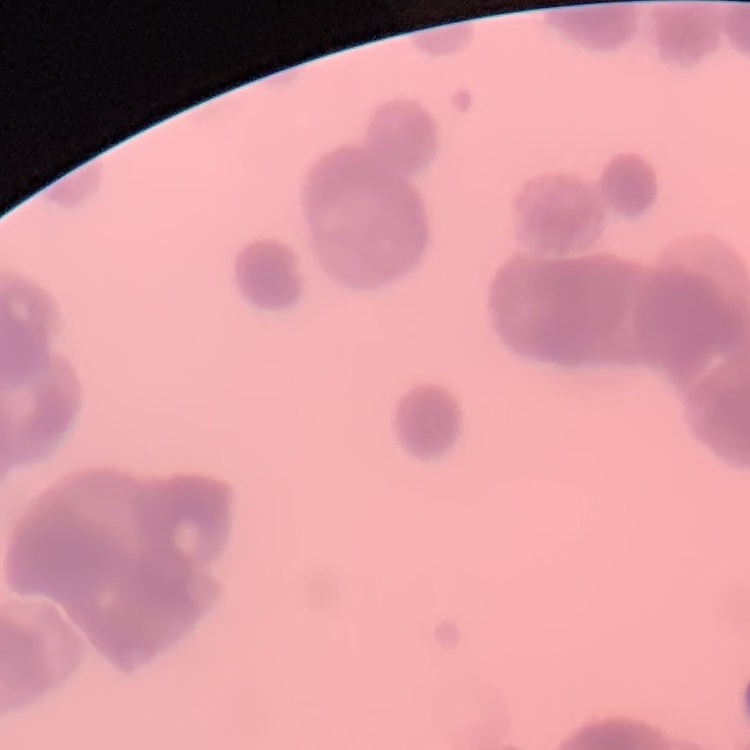 The red blood cells show rouleaux formation. Square crop of a larger photomicrograph. Thin peripheral smear. Stained with either Field's or Giemsa.